Assess this cell for malaria.
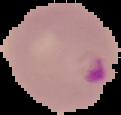
It is parasitized.

image size = 121×115 pixels
preparation = thin blood smear
image type = segmented cell region with the area outside set to black